State which parasite is depicted.
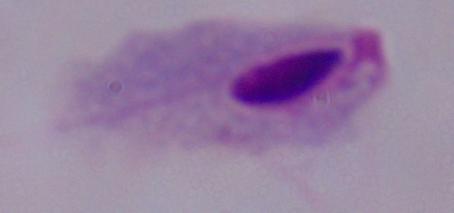
A trichomonad.

magnification = 1000x
modality = photomicrograph